Give the position of every leukocyte visible.
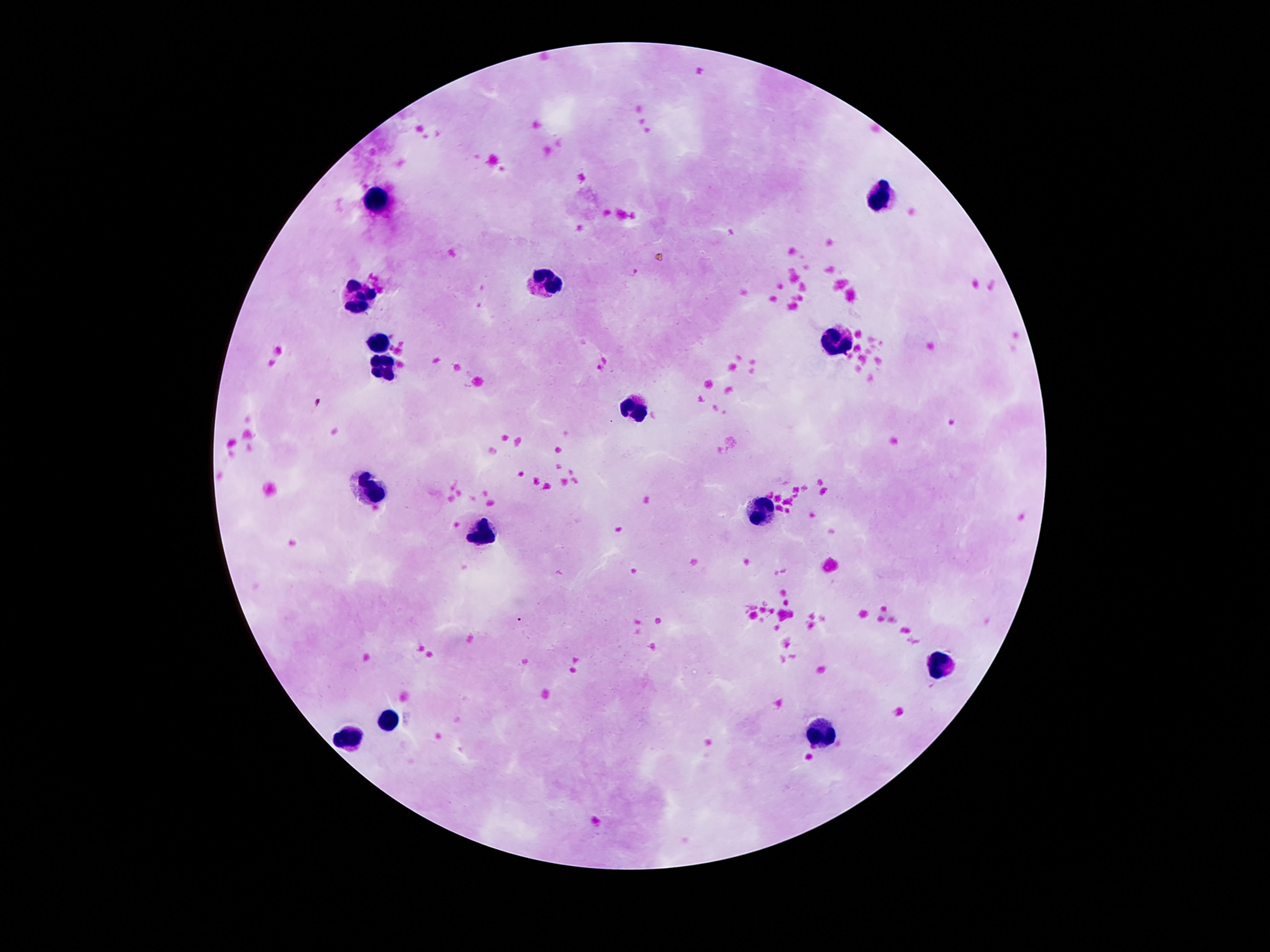

Approximate object centers, in pixels from the top-left corner.
Leukocytes: (x=879, y=196), (x=376, y=199), (x=544, y=280), (x=359, y=300), (x=380, y=338), (x=839, y=341), (x=384, y=364), (x=636, y=407), (x=369, y=488), (x=759, y=514), (x=482, y=532), (x=943, y=666), (x=389, y=720), (x=821, y=732), (x=348, y=739).

{
  "image_size": "1270×952 pixels",
  "capture": "smartphone camera through the microscope eyepiece",
  "preparation": "thick blood smear",
  "field_of_view": "single",
  "stain": "Giemsa",
  "patient_malaria_status": "negative",
  "magnification": "100x"
}